Give the extent of all Plasmodium vivax-infected red blood cells.
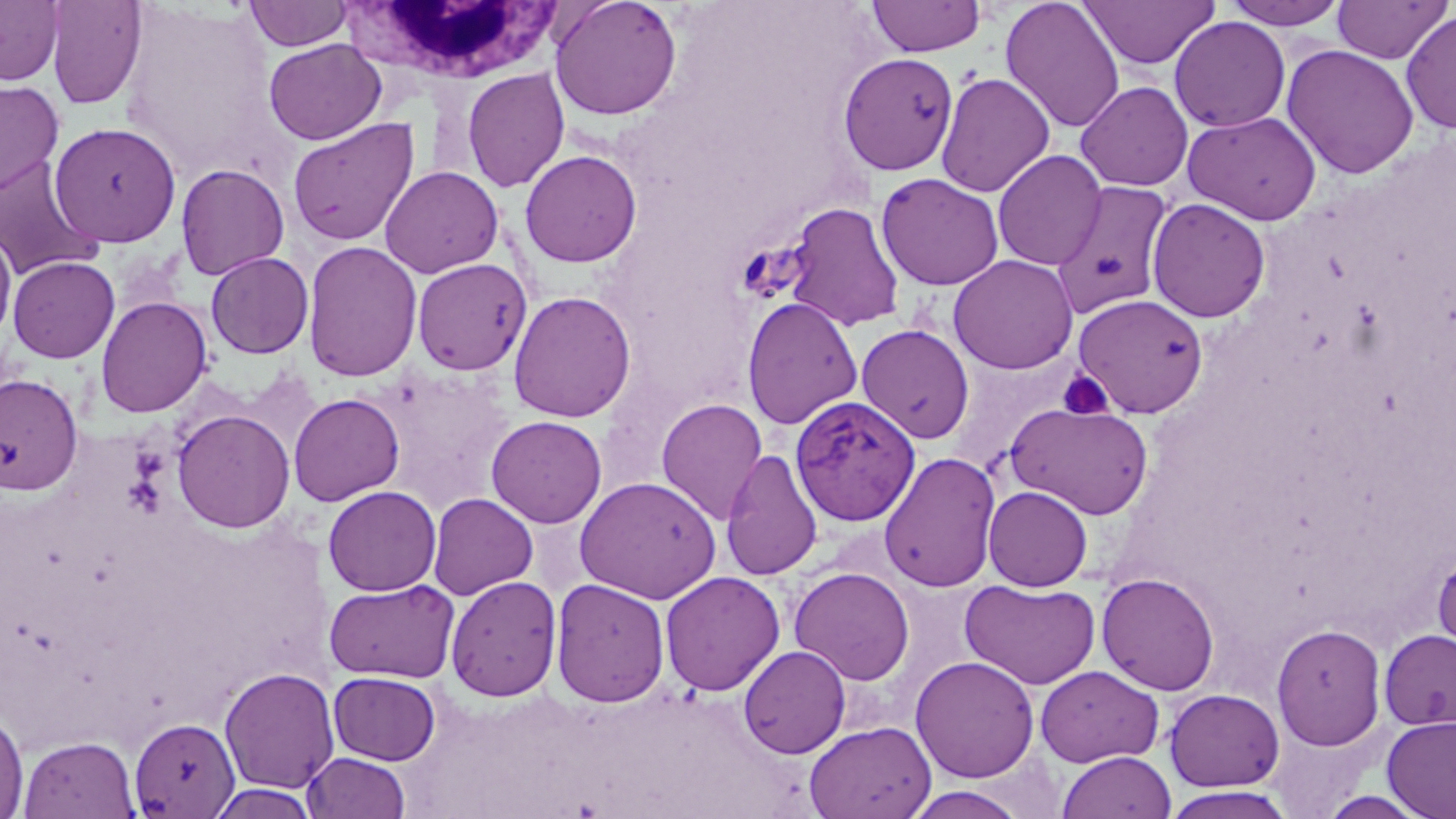

Approximate bounding boxes as named x1/y1/x2/y2 corners in pixels.
Plasmodium vivax-infected red blood cells: (x1=788, y1=394, x2=920, y2=527).

slide-level diagnosis = Plasmodium vivax
preparation = thin blood smear
field of view = one of a larger specimen
magnification = 1000x
white blood cell locations = approximate bounding boxes as named x1/y1/x2/y2 corners in pixels: (x1=343, y1=2, x2=567, y2=84)
stain = May-Grünwald-Giemsa
platelet locations = approximate bounding boxes as named x1/y1/x2/y2 corners in pixels: (x1=1057, y1=371, x2=1114, y2=420)
image size = 1456×819 pixels
uninfected red blood cell locations = approximate bounding boxes as named x1/y1/x2/y2 corners in pixels: (x1=0, y1=0, x2=63, y2=86), (x1=549, y1=0, x2=683, y2=120), (x1=867, y1=0, x2=986, y2=57), (x1=1000, y1=0, x2=1125, y2=133), (x1=1078, y1=0, x2=1219, y2=70), (x1=1221, y1=0, x2=1352, y2=30), (x1=1332, y1=0, x2=1451, y2=64), (x1=45, y1=1, x2=148, y2=110), (x1=244, y1=1, x2=354, y2=51), (x1=1305, y1=3, x2=1438, y2=139), (x1=1401, y1=10, x2=1456, y2=134), (x1=1169, y1=17, x2=1291, y2=133), (x1=264, y1=39, x2=386, y2=145), (x1=1281, y1=44, x2=1419, y2=179), (x1=837, y1=52, x2=959, y2=176), (x1=461, y1=67, x2=570, y2=193), (x1=936, y1=72, x2=1055, y2=198), (x1=0, y1=79, x2=64, y2=197), (x1=1075, y1=81, x2=1193, y2=191), (x1=1183, y1=111, x2=1321, y2=224), (x1=287, y1=117, x2=419, y2=247), (x1=48, y1=121, x2=182, y2=247), (x1=519, y1=149, x2=642, y2=267), (x1=992, y1=149, x2=1107, y2=270), (x1=0, y1=156, x2=102, y2=281), (x1=175, y1=163, x2=290, y2=280), (x1=379, y1=165, x2=504, y2=278), (x1=877, y1=173, x2=1004, y2=291), (x1=1051, y1=180, x2=1174, y2=317), (x1=1146, y1=198, x2=1271, y2=323), (x1=784, y1=202, x2=904, y2=332), (x1=0, y1=229, x2=17, y2=344), (x1=302, y1=240, x2=423, y2=383), (x1=205, y1=252, x2=314, y2=358), (x1=948, y1=254, x2=1078, y2=374), (x1=7, y1=256, x2=120, y2=363), (x1=412, y1=257, x2=533, y2=376), (x1=508, y1=290, x2=637, y2=422), (x1=1073, y1=293, x2=1208, y2=417), (x1=96, y1=296, x2=212, y2=418), (x1=741, y1=296, x2=862, y2=430), (x1=856, y1=324, x2=974, y2=444), (x1=0, y1=373, x2=83, y2=495), (x1=288, y1=393, x2=405, y2=506), (x1=656, y1=397, x2=768, y2=524), (x1=1004, y1=401, x2=1155, y2=519), (x1=172, y1=408, x2=295, y2=533), (x1=486, y1=415, x2=607, y2=528), (x1=720, y1=449, x2=823, y2=581), (x1=879, y1=452, x2=1001, y2=593), (x1=574, y1=476, x2=722, y2=603), (x1=322, y1=485, x2=441, y2=596), (x1=983, y1=485, x2=1093, y2=591), (x1=427, y1=493, x2=538, y2=600), (x1=1432, y1=549, x2=1456, y2=666), (x1=789, y1=566, x2=915, y2=685), (x1=660, y1=570, x2=785, y2=696), (x1=1097, y1=572, x2=1220, y2=695), (x1=445, y1=575, x2=562, y2=701), (x1=551, y1=578, x2=670, y2=708), (x1=324, y1=579, x2=459, y2=683), (x1=960, y1=579, x2=1101, y2=689), (x1=1271, y1=624, x2=1387, y2=751), (x1=1378, y1=629, x2=1456, y2=731), (x1=738, y1=645, x2=851, y2=758), (x1=910, y1=655, x2=1040, y2=782), (x1=1035, y1=665, x2=1163, y2=768), (x1=219, y1=666, x2=340, y2=794), (x1=328, y1=671, x2=441, y2=765), (x1=1164, y1=689, x2=1285, y2=792), (x1=0, y1=707, x2=29, y2=817), (x1=1381, y1=715, x2=1456, y2=819), (x1=128, y1=717, x2=240, y2=817), (x1=804, y1=720, x2=936, y2=819), (x1=18, y1=735, x2=140, y2=818), (x1=1057, y1=751, x2=1176, y2=819), (x1=302, y1=752, x2=411, y2=819), (x1=207, y1=784, x2=322, y2=819), (x1=902, y1=786, x2=1029, y2=819), (x1=1161, y1=787, x2=1298, y2=818)
modality = optical microscopy